Comment on the morphology of the erythrocytes.
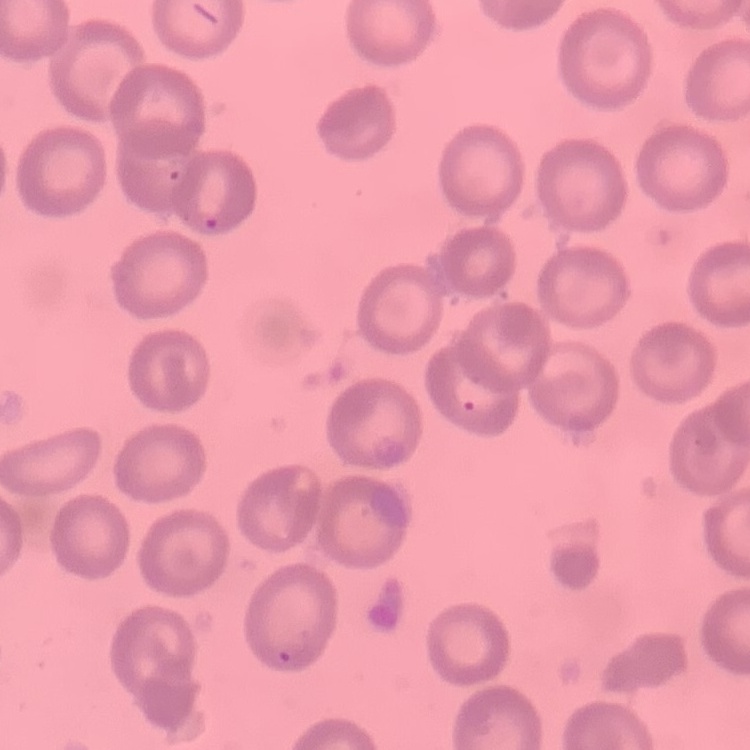

No rouleaux formation.

preparation = thin blood smear
image type = square crop of a larger photomicrograph
stain = Field's or Giemsa